Outline each blood parasite and name the species.
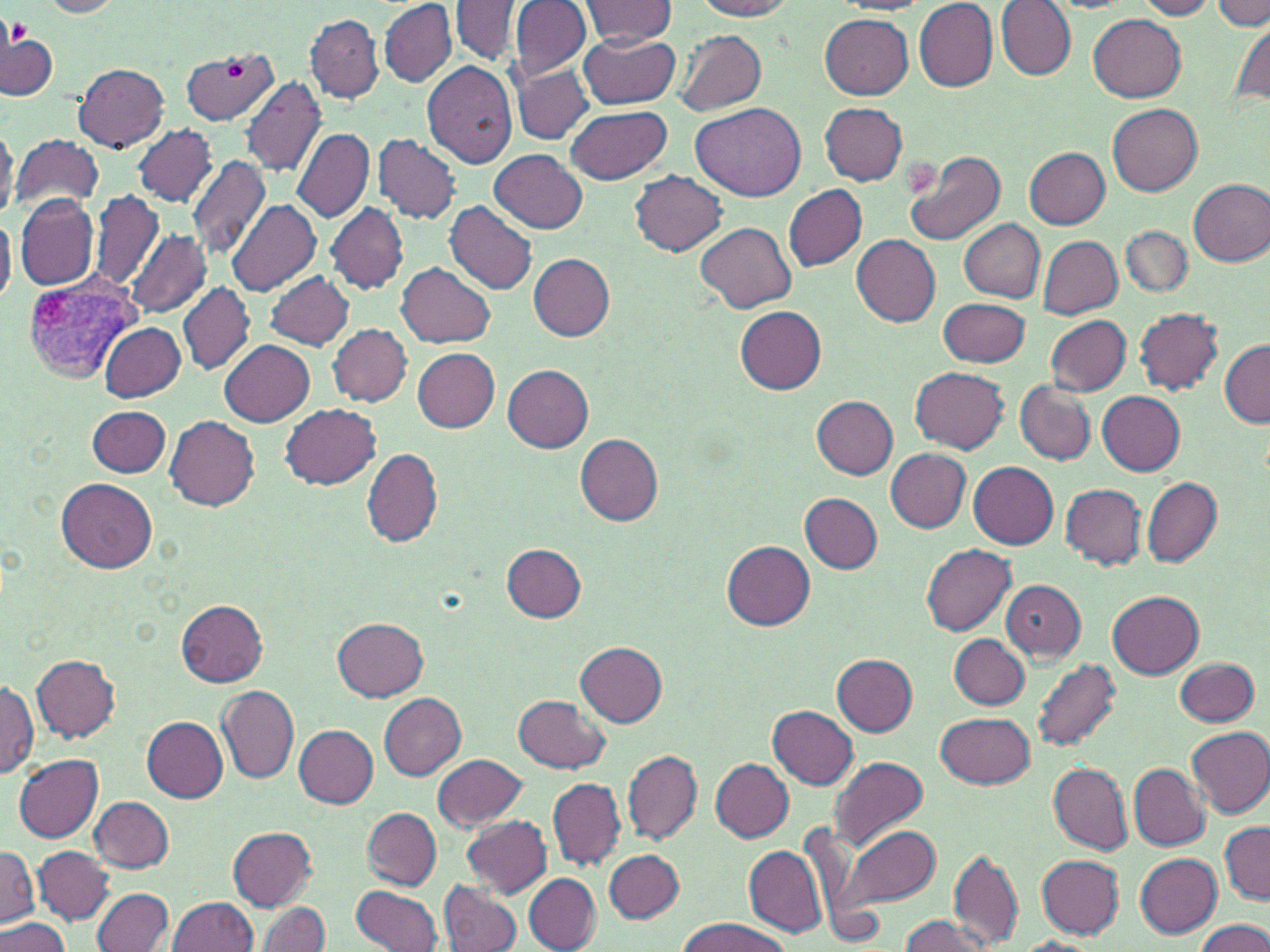
Approximate bounding boxes as named x1/y1/x2/y2 corners in pixels.
Plasmodium vivax-infected red blood cells: (x1=21, y1=268, x2=147, y2=382).
No Plasmodium falciparum, Plasmodium ovale, Plasmodium malariae, Babesia divergens, or Trypanosoma brucei observed.

Summary:
  - Platelet locations: (x1=7, y1=20, x2=30, y2=45), (x1=225, y1=61, x2=244, y2=79)
  - Uninfected red blood cell locations: (x1=379, y1=0, x2=456, y2=86), (x1=694, y1=0, x2=793, y2=20), (x1=914, y1=0, x2=998, y2=90), (x1=1137, y1=0, x2=1218, y2=19), (x1=42, y1=1, x2=125, y2=17), (x1=452, y1=1, x2=521, y2=64), (x1=509, y1=1, x2=591, y2=82), (x1=580, y1=1, x2=677, y2=45), (x1=1214, y1=1, x2=1268, y2=29), (x1=996, y1=2, x2=1075, y2=81), (x1=306, y1=14, x2=383, y2=102), (x1=820, y1=14, x2=913, y2=99), (x1=1088, y1=15, x2=1186, y2=102), (x1=1228, y1=19, x2=1270, y2=110), (x1=578, y1=28, x2=681, y2=109), (x1=674, y1=29, x2=765, y2=115), (x1=2, y1=31, x2=57, y2=101), (x1=180, y1=47, x2=278, y2=123), (x1=74, y1=62, x2=168, y2=151), (x1=421, y1=62, x2=517, y2=170), (x1=512, y1=65, x2=593, y2=143), (x1=241, y1=76, x2=326, y2=177), (x1=1107, y1=101, x2=1203, y2=196), (x1=691, y1=102, x2=807, y2=200), (x1=819, y1=103, x2=907, y2=185), (x1=567, y1=104, x2=671, y2=185), (x1=0, y1=120, x2=17, y2=222), (x1=134, y1=124, x2=217, y2=206), (x1=292, y1=127, x2=373, y2=224), (x1=14, y1=134, x2=102, y2=212), (x1=375, y1=135, x2=462, y2=223), (x1=1025, y1=147, x2=1110, y2=227), (x1=903, y1=149, x2=1006, y2=247), (x1=489, y1=151, x2=587, y2=233), (x1=185, y1=156, x2=270, y2=260), (x1=630, y1=170, x2=726, y2=256), (x1=1188, y1=178, x2=1270, y2=266), (x1=785, y1=185, x2=867, y2=272), (x1=88, y1=190, x2=165, y2=292), (x1=15, y1=194, x2=98, y2=292), (x1=226, y1=198, x2=322, y2=297), (x1=445, y1=201, x2=537, y2=294), (x1=325, y1=204, x2=407, y2=293), (x1=0, y1=211, x2=16, y2=308), (x1=959, y1=218, x2=1045, y2=303), (x1=696, y1=222, x2=795, y2=312), (x1=1122, y1=225, x2=1192, y2=297), (x1=127, y1=228, x2=211, y2=318), (x1=851, y1=234, x2=940, y2=326), (x1=1037, y1=235, x2=1122, y2=318), (x1=528, y1=253, x2=614, y2=340), (x1=397, y1=262, x2=495, y2=349), (x1=265, y1=271, x2=354, y2=350), (x1=178, y1=281, x2=255, y2=375), (x1=939, y1=296, x2=1030, y2=368), (x1=735, y1=306, x2=828, y2=394), (x1=1134, y1=307, x2=1223, y2=394), (x1=1045, y1=315, x2=1131, y2=395), (x1=99, y1=322, x2=183, y2=401), (x1=327, y1=323, x2=411, y2=406), (x1=219, y1=340, x2=314, y2=425), (x1=1219, y1=340, x2=1270, y2=428), (x1=412, y1=347, x2=499, y2=432), (x1=502, y1=364, x2=593, y2=452), (x1=911, y1=365, x2=1009, y2=453), (x1=1014, y1=380, x2=1096, y2=466), (x1=1096, y1=389, x2=1185, y2=474), (x1=810, y1=396, x2=898, y2=478), (x1=281, y1=403, x2=381, y2=488), (x1=88, y1=406, x2=170, y2=478), (x1=166, y1=415, x2=260, y2=513), (x1=575, y1=435, x2=664, y2=525), (x1=362, y1=447, x2=442, y2=546), (x1=884, y1=447, x2=970, y2=532), (x1=880, y1=454, x2=1050, y2=538), (x1=968, y1=462, x2=1057, y2=549), (x1=1141, y1=475, x2=1221, y2=567), (x1=57, y1=477, x2=157, y2=573), (x1=1061, y1=483, x2=1146, y2=568), (x1=800, y1=493, x2=882, y2=573), (x1=723, y1=541, x2=816, y2=630), (x1=503, y1=543, x2=586, y2=622), (x1=921, y1=544, x2=1016, y2=635), (x1=1001, y1=580, x2=1085, y2=660), (x1=1107, y1=590, x2=1204, y2=675), (x1=175, y1=599, x2=268, y2=687), (x1=332, y1=617, x2=428, y2=700), (x1=950, y1=634, x2=1030, y2=708), (x1=577, y1=642, x2=666, y2=726), (x1=832, y1=654, x2=918, y2=735), (x1=32, y1=656, x2=120, y2=742), (x1=1175, y1=657, x2=1260, y2=726), (x1=1031, y1=659, x2=1121, y2=751), (x1=0, y1=677, x2=38, y2=779), (x1=217, y1=685, x2=299, y2=783), (x1=378, y1=693, x2=466, y2=780), (x1=514, y1=694, x2=608, y2=772), (x1=769, y1=705, x2=858, y2=789), (x1=936, y1=711, x2=1034, y2=789), (x1=143, y1=716, x2=226, y2=802), (x1=295, y1=724, x2=378, y2=808), (x1=1187, y1=726, x2=1270, y2=817), (x1=623, y1=749, x2=702, y2=845), (x1=13, y1=754, x2=104, y2=842), (x1=433, y1=754, x2=527, y2=831), (x1=829, y1=756, x2=929, y2=850), (x1=711, y1=758, x2=793, y2=842), (x1=549, y1=761, x2=705, y2=852), (x1=1048, y1=763, x2=1132, y2=854), (x1=1129, y1=764, x2=1209, y2=849), (x1=548, y1=777, x2=625, y2=870), (x1=91, y1=796, x2=175, y2=872), (x1=363, y1=807, x2=441, y2=889), (x1=461, y1=815, x2=553, y2=898), (x1=1220, y1=821, x2=1269, y2=904), (x1=833, y1=822, x2=942, y2=912), (x1=227, y1=827, x2=318, y2=910), (x1=744, y1=845, x2=827, y2=937), (x1=1, y1=846, x2=38, y2=926), (x1=33, y1=846, x2=113, y2=923), (x1=604, y1=849, x2=684, y2=922), (x1=949, y1=849, x2=1023, y2=947), (x1=1134, y1=852, x2=1223, y2=937), (x1=1036, y1=854, x2=1125, y2=938), (x1=524, y1=874, x2=601, y2=951), (x1=439, y1=879, x2=523, y2=952), (x1=353, y1=884, x2=443, y2=952), (x1=93, y1=888, x2=173, y2=951), (x1=168, y1=896, x2=259, y2=952), (x1=258, y1=901, x2=330, y2=952), (x1=899, y1=914, x2=996, y2=952), (x1=0, y1=917, x2=70, y2=952), (x1=677, y1=918, x2=790, y2=952), (x1=1194, y1=920, x2=1270, y2=952), (x1=1016, y1=938, x2=1102, y2=952)
  - Slide-level diagnosis: Plasmodium vivax
  - Field of view: single
  - Modality: optical microscopy
  - Stain: May-Grünwald-Giemsa
  - Image size: 1270×952 pixels
  - Magnification: 1000x
  - Preparation: thin blood film